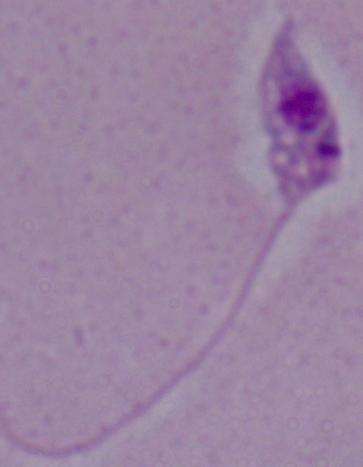
modality = photomicrograph
magnification = 1000x
identification = Leishmania